State which parasite is depicted.
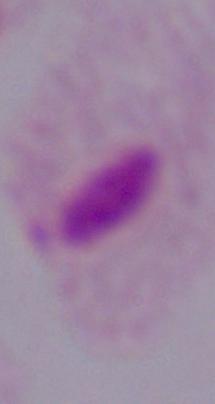

This is a trichomonad.

modality = photomicrograph
magnification = 1000x